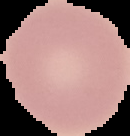
Malaria status: uninfected. Segmented cell region on a black background. Image is 130×136 pixels. From a thin blood film.